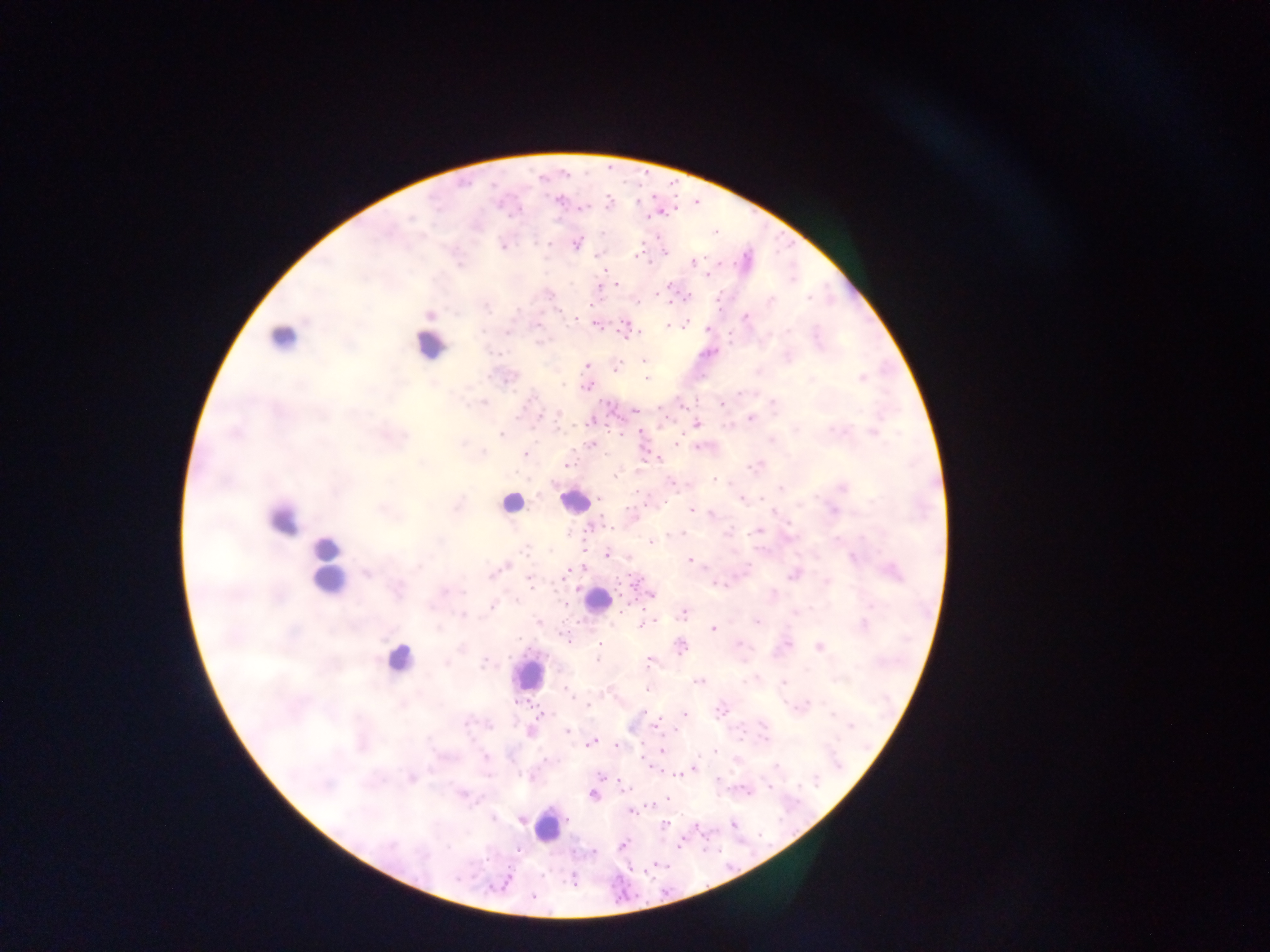

Approximate centers as [x, y] in pixels. Leukocyte locations: [282, 339], [430, 344], [573, 501], [510, 502], [281, 518], [327, 567], [596, 601], [397, 659], [527, 674], [548, 825]. Malaria parasite locations: [558, 200], [609, 201], [581, 208], [664, 213], [410, 218], [715, 231], [576, 243], [549, 244], [503, 248], [665, 252], [596, 255], [637, 256], [693, 263], [708, 274], [616, 284], [598, 286], [670, 286], [688, 295], [807, 297], [771, 301], [637, 303], [668, 303], [430, 316], [746, 316], [575, 319], [595, 324], [685, 324], [537, 326], [668, 326], [707, 329], [624, 332], [640, 332], [507, 333], [644, 360], [586, 366], [616, 368], [861, 378], [646, 379], [811, 379], [562, 385], [586, 387], [739, 393], [772, 403], [721, 404], [635, 410], [558, 414], [750, 418], [589, 422], [697, 424], [832, 428], [639, 430], [873, 433], [501, 435], [676, 444], [591, 445], [483, 452], [526, 454], [658, 459], [567, 465], [750, 467], [615, 475], [714, 479], [671, 483], [843, 487], [781, 488], [761, 498], [600, 499], [742, 499], [871, 501], [628, 508], [692, 510], [833, 511], [711, 514], [588, 528], [756, 531], [683, 533], [675, 534], [651, 542], [525, 549], [608, 555], [853, 557], [689, 560], [505, 566], [566, 572], [893, 572], [366, 574], [792, 576], [826, 581], [530, 582], [651, 595], [565, 605], [491, 607], [795, 613], [684, 615], [462, 616], [538, 621], [756, 621], [650, 622], [645, 624], [864, 624], [713, 629], [564, 637], [787, 643], [599, 644], [681, 647], [741, 647], [819, 647], [597, 660], [649, 661], [485, 662], [698, 681], [784, 683], [566, 688], [648, 689], [587, 704], [721, 711], [643, 712], [541, 714], [684, 714], [832, 714], [489, 725], [851, 725], [566, 730], [530, 732], [591, 743], [617, 745], [662, 751], [715, 752], [486, 757], [777, 766], [694, 768], [679, 774], [602, 777], [411, 778], [717, 779], [816, 782], [768, 787], [463, 794], [592, 794], [667, 799], [630, 812], [494, 818], [521, 819], [665, 825], [734, 825], [679, 844], [623, 845], [517, 850], [593, 852], [573, 881], [533, 897]. Thick blood smear. Mobile-phone photograph taken through the microscope. Image is 1270×952 pixels. Sample from Ghana. Single field of view.